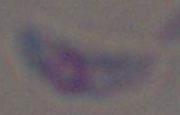

{
  "modality": "micrograph",
  "identification": "Toxoplasma gondii",
  "magnification": "1000x"
}